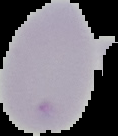
preparation = thin blood smear
image size = 118×136 pixels
result = negative for Plasmodium parasites
image type = segmented cell region on a black background